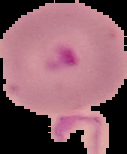

Summary:
  - Preparation: thin blood film
  - Image size: 127×154 pixels
  - Image type: segmented cell region on a black background
  - Result: Plasmodium parasites identified